Locate every Plasmodium parasite.
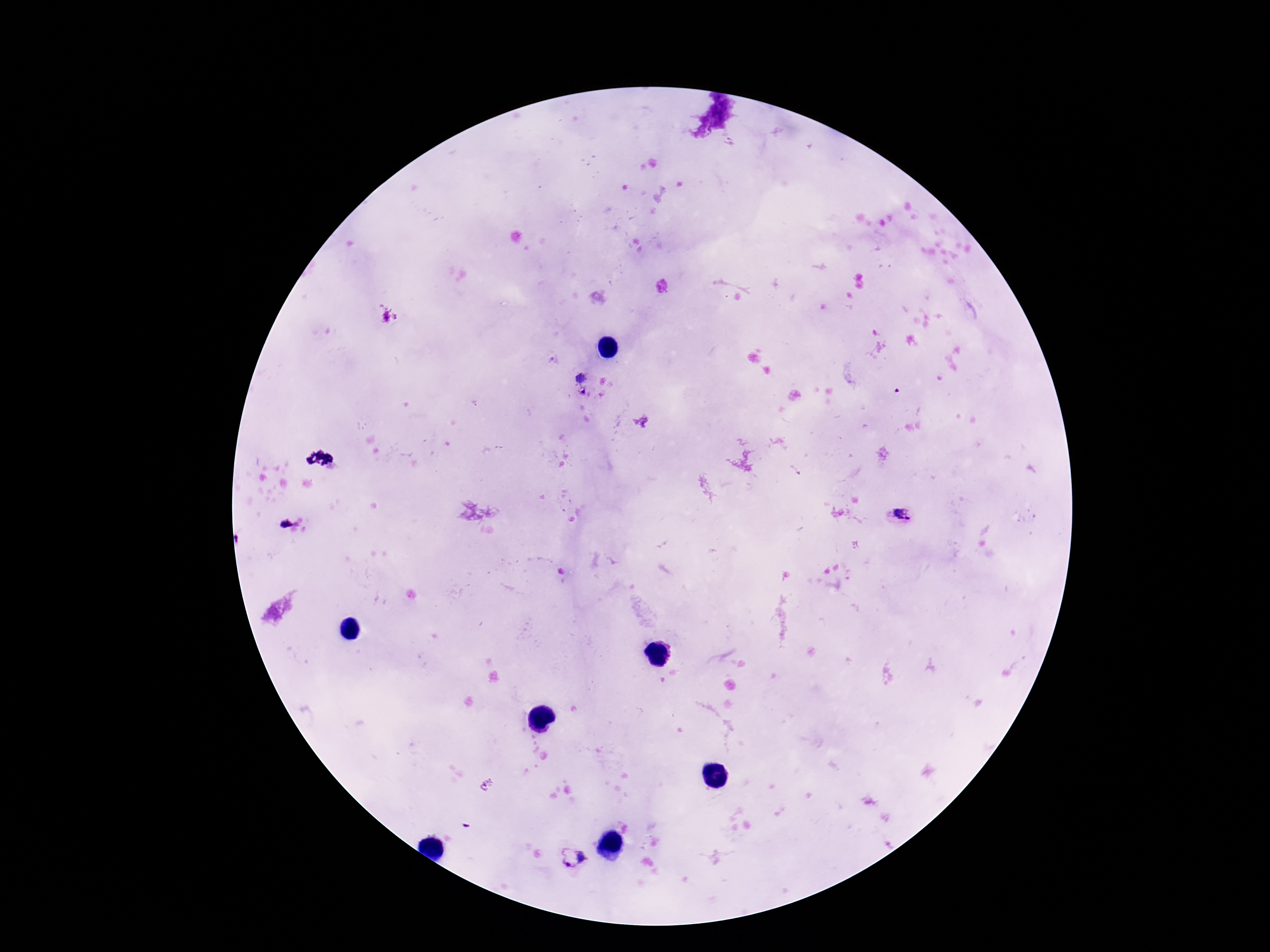

Approximate centers as (x, y) in pixels.
Plasmodium parasites: (579, 384), (900, 516), (572, 858).

100x magnification. Image is 1270×952 pixels. Patient malaria status: positive. Giemsa stain. Single field of view. Smartphone photograph taken through the microscope eyepiece. Thick blood film.